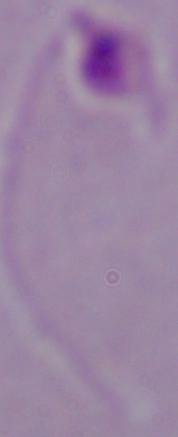
identification = Leishmania
modality = photomicrograph
magnification = 1000x